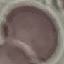
malaria status = uninfected
capture = smartphone through the microscope eyepiece
image type = automatically extracted cell patch, resized to 64 × 64 pixels
preparation = thin blood film
stain = Giemsa